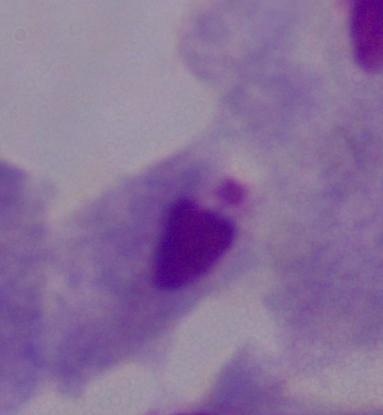
identification: trichomonad
modality: micrograph
magnification: 1000x